Name the cell type shown.
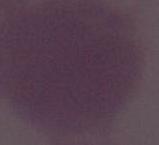
An erythrocyte.

Summary:
  - Magnification: 1000x
  - Modality: photomicrograph